State which parasite is depicted.
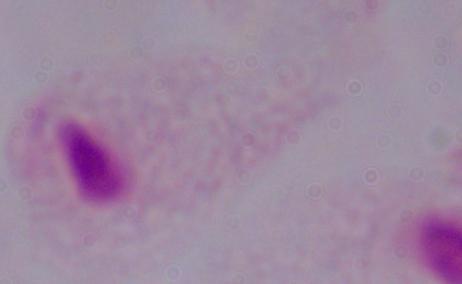
This is a trichomonad.

modality = photomicrograph
magnification = 1000x